State which cell type is depicted.
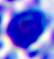
A leukocyte.

modality = micrograph
magnification = 400x